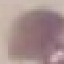 Result: no malaria parasites seen. Acquired by smartphone through the microscope eyepiece. Cell patch, automatically extracted from a larger field of view and resized to 64 × 64 pixels. Giemsa-stained preparation. Thin blood smear.